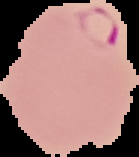

preparation = thin blood film
image type = cell region segmented out of the field of view; surrounding area masked to black
image size = 139×157 pixels
result = Plasmodium parasites identified